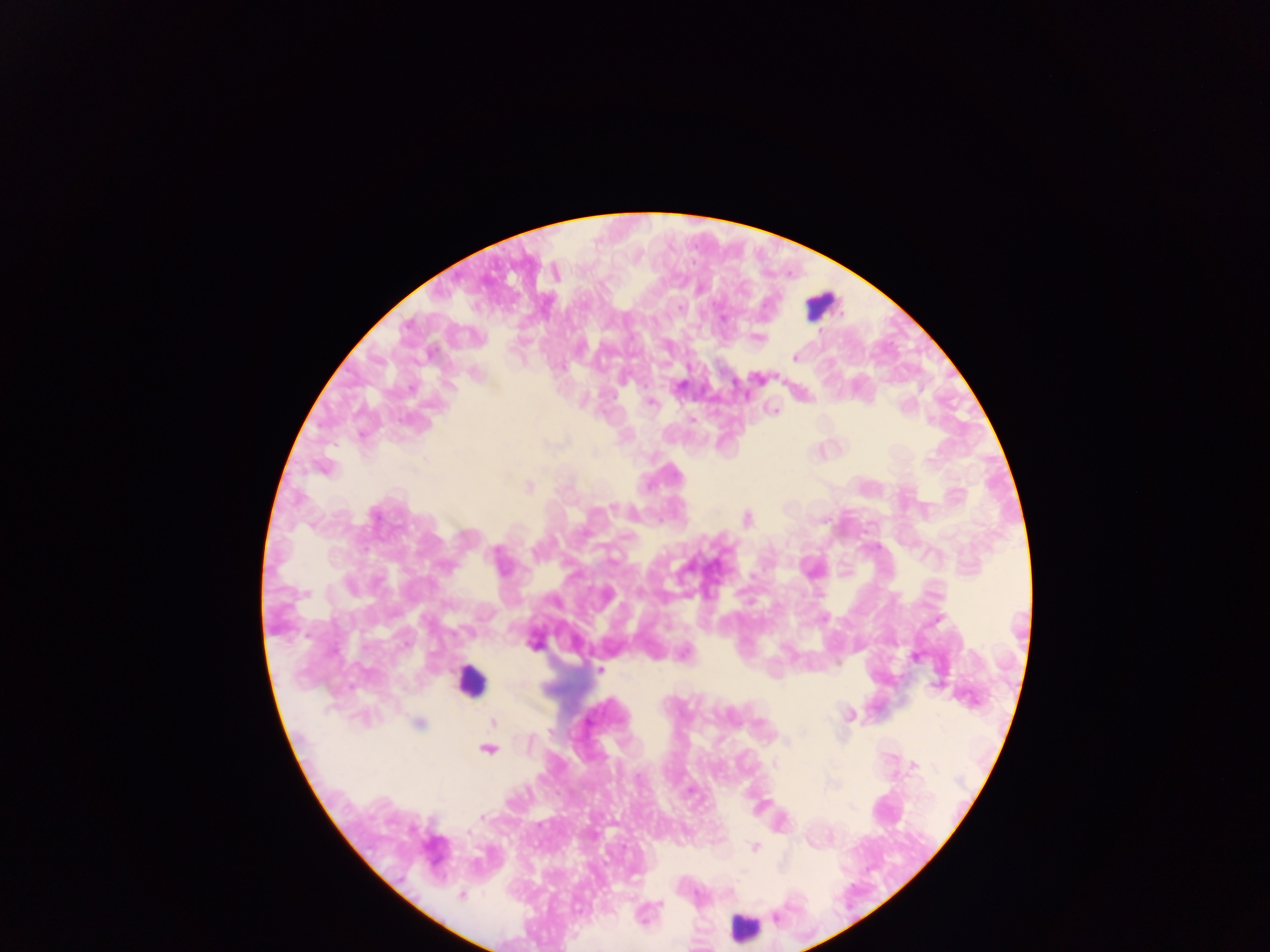 Approximate centers as [x, y] in pixels. Plasmodium parasite locations: [680, 307], [723, 318], [758, 338], [795, 357], [624, 382], [680, 385], [652, 403], [904, 406], [774, 411], [692, 420], [931, 420], [930, 460], [528, 486], [613, 507], [375, 516], [747, 518], [497, 550], [446, 567], [533, 643], [915, 657], [600, 669], [849, 716], [493, 721], [419, 723], [760, 723], [550, 731], [529, 742], [488, 750], [775, 764], [913, 765], [482, 817], [467, 833], [754, 847], [461, 895], [659, 904], [775, 916]. Leukocyte locations: [819, 306], [470, 680], [742, 928]. Thick blood film. Collected in Ghana. Single field of view. Mobile-phone photograph taken through the microscope. Image is 1270×952 pixels.